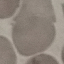

{
  "malaria_status": "uninfected",
  "image_type": "automatically extracted cell patch, resized to 64 × 64 pixels",
  "stain": "Giemsa",
  "capture": "smartphone camera at the microscope eyepiece",
  "preparation": "thin blood film"
}